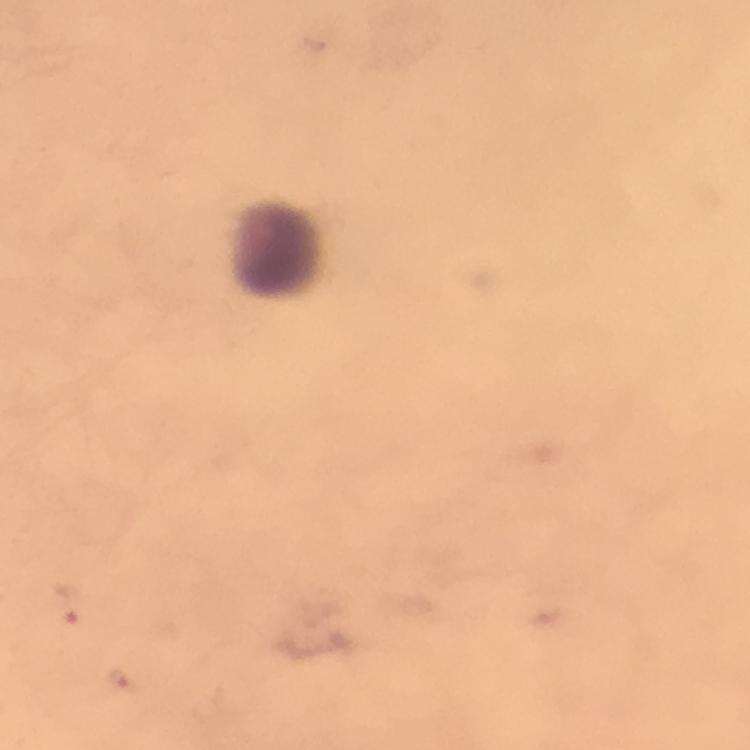
Approximate centers as {x, y} in pixels.
Summary:
  - Plasmodium parasite locations: {65, 605}, {118, 680}
  - Leukocyte locations: {281, 251}
  - Capture: smartphone photograph through a microscope
  - Image size: 750×750 pixels
  - Stain: Giemsa
  - Magnification: 100x
  - Preparation: thick blood film
  - Immersion oil: applied
  - Context: from a diagnostic examination for malaria
  - Cropped from: one field of view